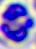

Captured at 400x magnification. Photomicrograph. A white blood cell is seen.